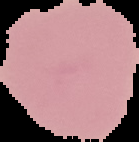 Cell region segmented out of the field of view; the surrounding area is masked to black. From a thin blood film. Image is 139×142 pixels. Result: no malaria parasites detected.